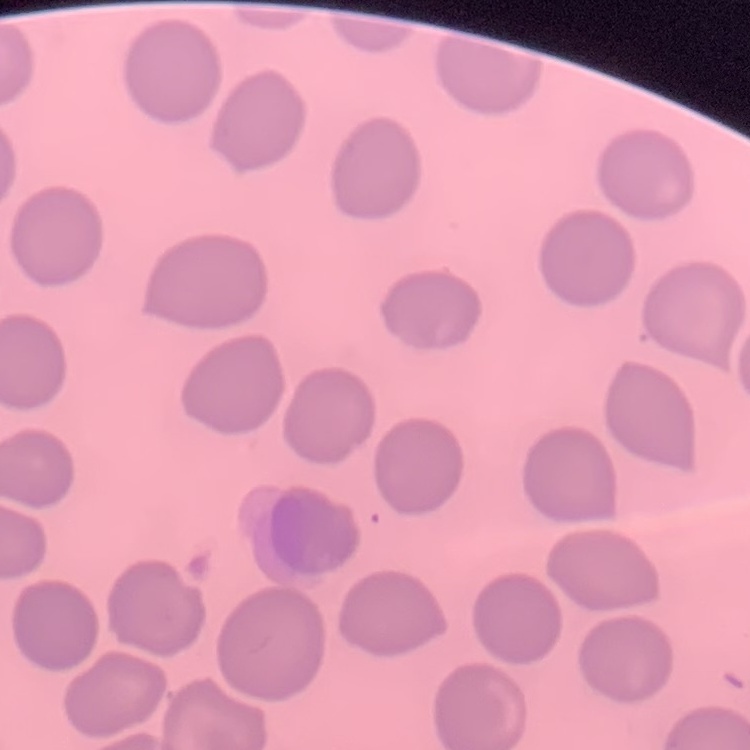 The red blood cells show no rouleaux formation. Stained with either Field's or Giemsa. Thin blood smear. One tile cut from a larger photomicrograph.